Name the parasite shown.
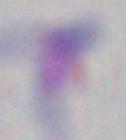
This is Toxoplasma gondii.

magnification: 1000x
modality: photomicrograph